Assess this cell for malaria.
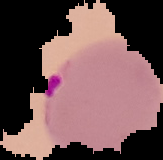
It is parasitized.

Summary:
  - Image type: cell region segmented out of the field of view; surrounding area masked to black
  - Preparation: thin blood film
  - Image size: 163×160 pixels